Outline each blood parasite and name the species.
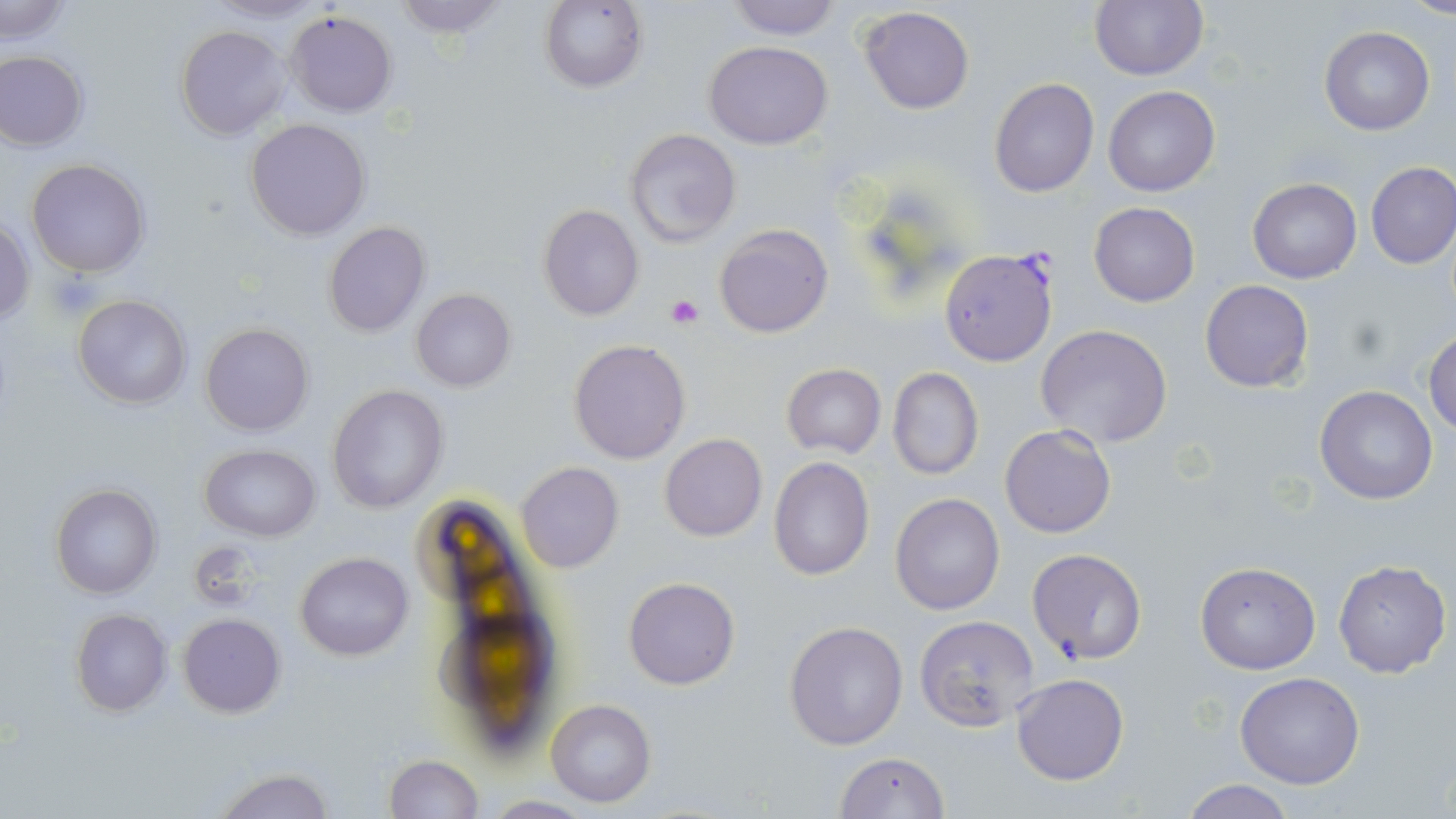
Approximate bounding boxes as (x1,y1)-(x2,y2) corner pairs in pixels.
Plasmodium falciparum-infected red blood cells: (939,248)-(1059,367).
No Plasmodium ovale, Plasmodium malariae, Plasmodium vivax, Babesia divergens, or Trypanosoma brucei observed.

slide_level_diagnosis: Plasmodium falciparum
image_size: 1456×819 pixels
field_of_view: one of a larger specimen
uninfected_red_blood_cell_locations: 'approximate bounding boxes as (x1,y1)-(x2,y2) corner pairs in pixels: (205,0)-(332,22), (390,0)-(509,39), (539,0)-(647,93), (726,0)-(842,40), (1,1)-(74,42), (1089,1)-(1208,80), (859,6)-(975,114), (284,10)-(398,117), (174,24)-(290,139), (1319,26)-(1435,136), (703,40)-(834,150), (0,50)-(88,151), (989,77)-(1099,198), (1103,85)-(1220,197), (245,118)-(369,240), (626,127)-(742,248), (27,159)-(149,278), (1365,161)-(1456,268), (1248,177)-(1362,284), (1088,202)-(1200,306), (538,204)-(644,321), (0,218)-(34,329), (323,222)-(430,336), (714,223)-(834,337), (1199,279)-(1315,392), (411,289)-(515,393), (72,294)-(192,408), (201,322)-(313,436), (1035,323)-(1173,448), (1423,330)-(1456,435), (568,339)-(690,463), (781,364)-(886,458), (886,366)-(984,481), (327,385)-(449,514), (1314,385)-(1439,504), (999,423)-(1116,539), (659,434)-(767,541), (200,444)-(320,540), (768,456)-(875,581), (516,462)-(624,574), (51,483)-(161,599), (889,492)-(1005,615), (1026,547)-(1148,664), (295,552)-(414,660), (1332,559)-(1451,679), (1195,562)-(1321,674), (624,577)-(740,689), (70,609)-(172,715), (177,613)-(286,717), (913,615)-(1039,733), (784,621)-(909,750), (1234,673)-(1365,790), (1012,674)-(1128,786), (546,699)-(656,807), (833,752)-(948,818), (383,755)-(484,819), (211,765)-(335,819), (1178,779)-(1297,818)'
stain: May-Grünwald-Giemsa
modality: light microscopy
preparation: thin blood film
platelet_locations: 'approximate bounding boxes as (x1,y1)-(x2,y2) corner pairs in pixels: (47,272)-(102,319), (668,296)-(703,328)'
magnification: 1000x